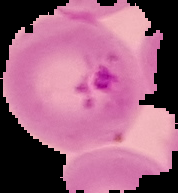 Malaria status: parasitized. From a thin blood film. Segmented cell region on a black background. Image is 178×193 pixels.